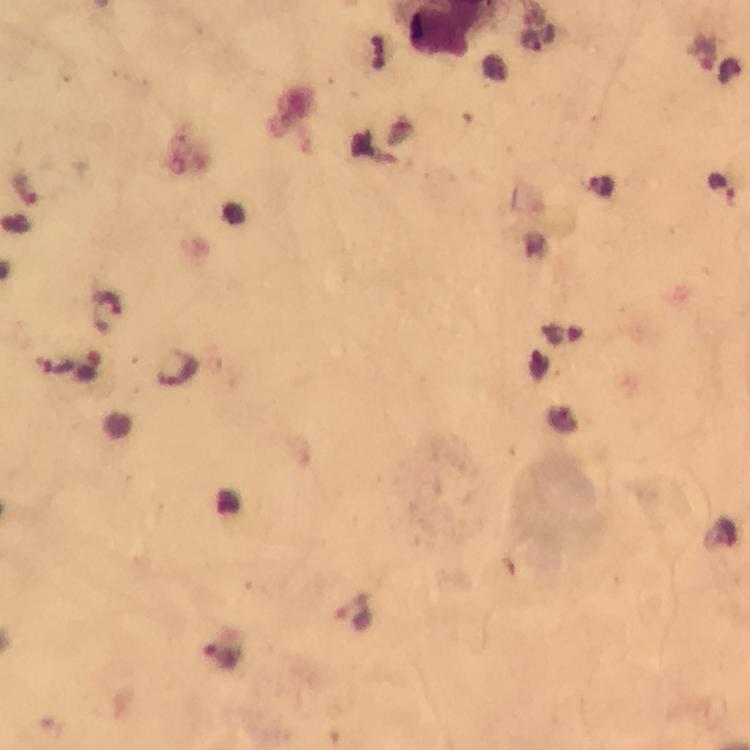
immersion oil = applied
capture = smartphone photograph through a microscope
preparation = thick blood film
image size = 750×750 pixels
magnification = 100x
stain = Giemsa
Plasmodium parasite locations = approximate centers as {x, y} in pixels: {532, 42}, {721, 186}, {602, 187}, {176, 369}, {355, 613}, {220, 654}
cropped from = one field of view
context = from a malaria diagnostic workup